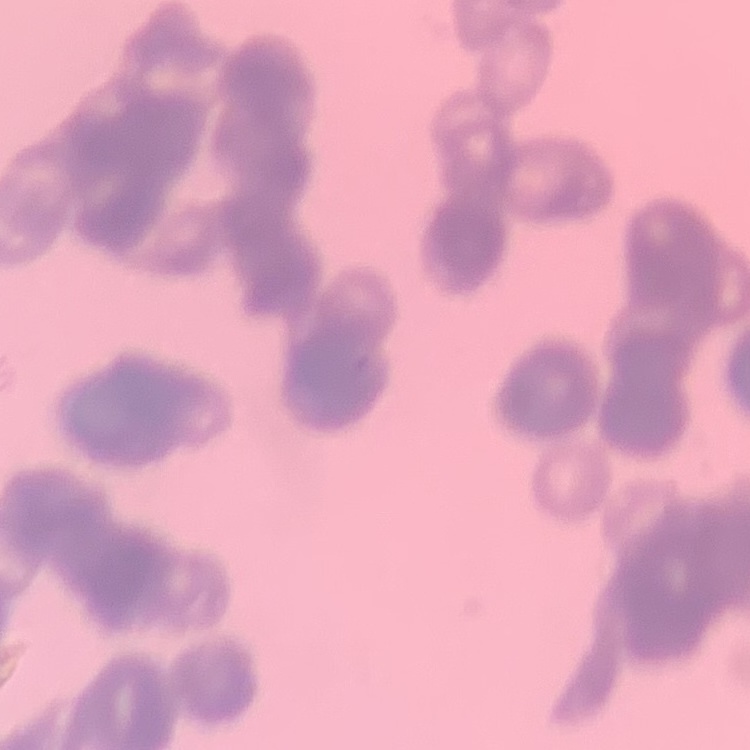
The red blood cells exhibit rouleaux formation. Field's or Giemsa stain. One tile cut from a larger photomicrograph. Thin peripheral smear.